Report the malaria status of this cell.
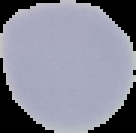
It is uninfected.

preparation: thin blood film
image_size: 136×133 pixels
image_type: segmented cell region on a black background